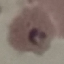
Summary:
  - Malaria status: parasitized
  - Stain: Giemsa
  - Image type: automatically extracted cell patch, resized to 64 × 64 pixels
  - Preparation: thin blood smear
  - Capture: smartphone through the microscope eyepiece